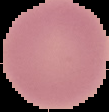
Summary:
  - Image size: 109×112 pixels
  - Image type: cell region segmented out of the field of view; surrounding area masked to black
  - Preparation: thin blood film
  - Result: negative for malaria parasites